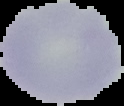 From a thin blood film. Result: no Plasmodium parasites detected. Image is 124×106 pixels. Segmented cell region on a black background.